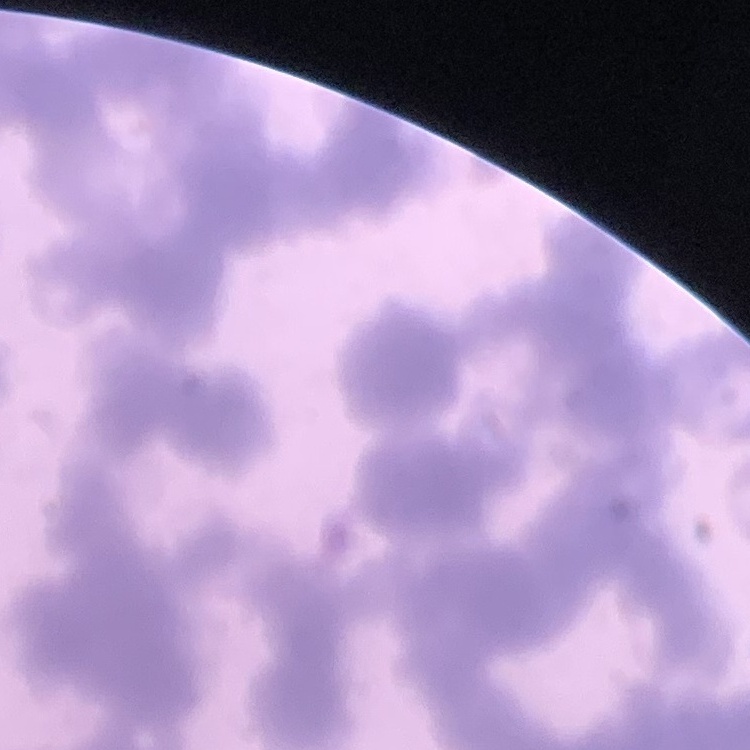 The erythrocytes show rouleaux formation. Field's or Giemsa stain. Thin peripheral smear. One tile cut from a larger photomicrograph.